Name the parasite shown.
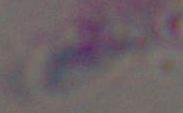

This is Toxoplasma gondii.

magnification: 1000x
modality: photomicrograph